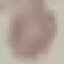 Malaria status: uninfected. Cell patch, automatically extracted from a larger field of view and resized to 64 × 64 pixels. Thin blood smear. Photographed with a smartphone camera at the microscope eyepiece. Giemsa-stained preparation.